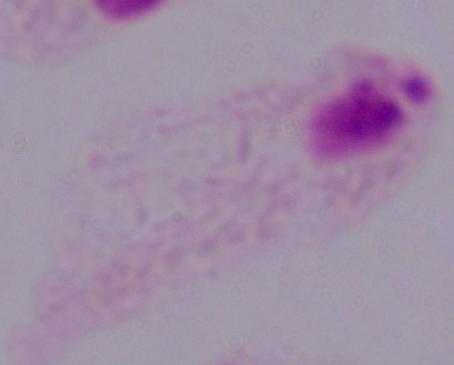

{
  "identification": "trichomonad",
  "modality": "micrograph",
  "magnification": "1000x"
}